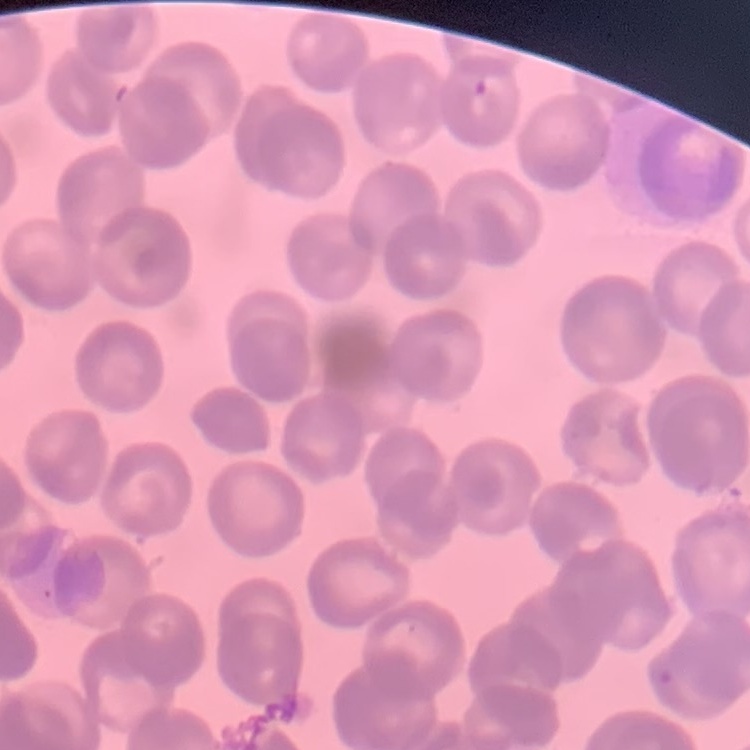

Summary:
  - Erythrocyte morphology: rouleaux formation
  - Preparation: thin blood film
  - Image type: one tile cut from a larger photomicrograph
  - Stain: Field's or Giemsa